Classify this cell by malaria status.
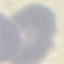

Uninfected.

Giemsa-stained preparation. Photographed with a smartphone camera at the microscope eyepiece. Automatically extracted cell patch, resized to 64 × 64 pixels. Thin blood film.